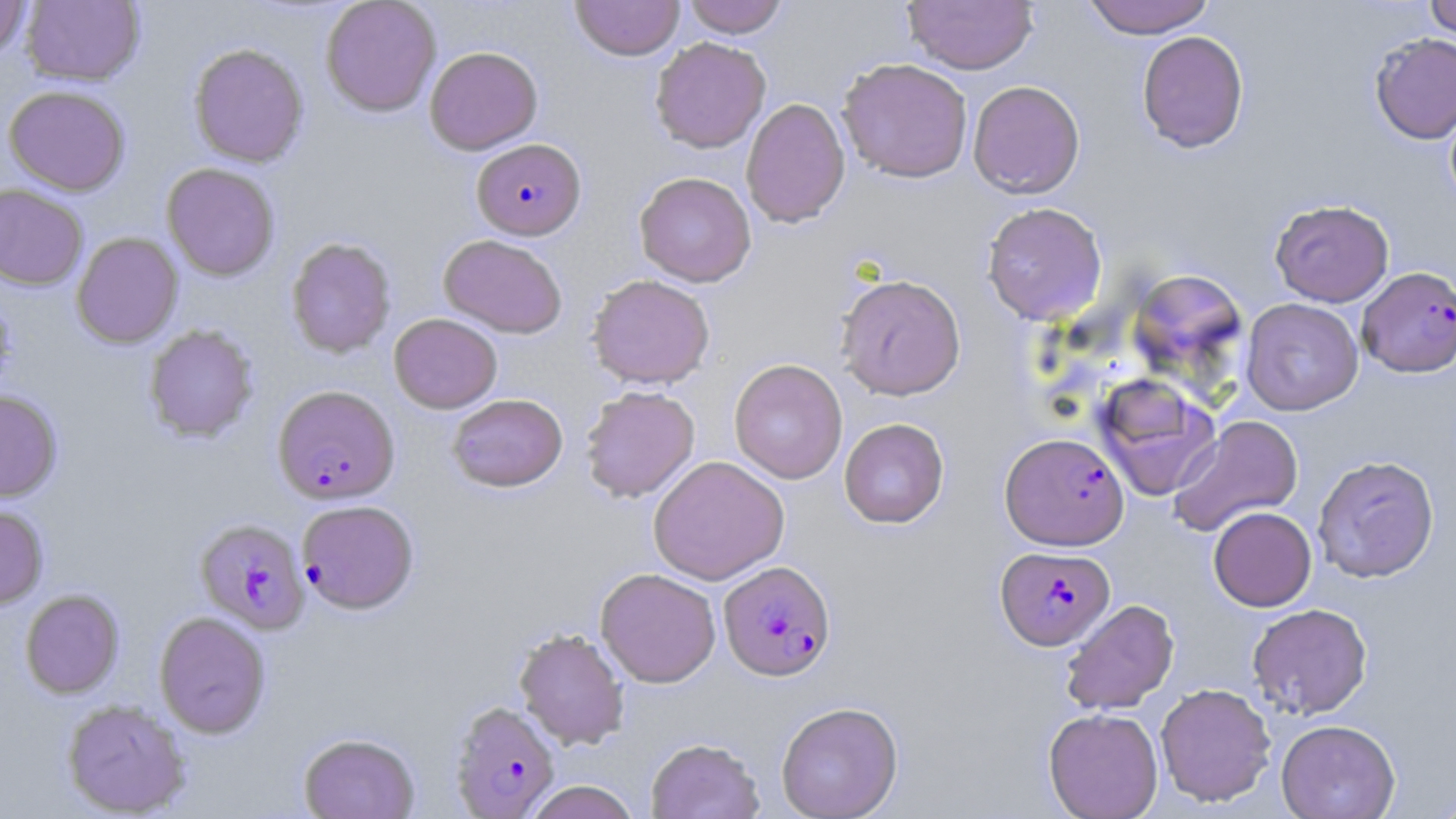

Summary:
  - Coordinate format: approximate bounding boxes as (x1, y1, x2, y2) in pixels
  - Uninfected red blood cell locations: (0, 0, 32, 61), (320, 0, 442, 117), (571, 0, 684, 61), (682, 0, 790, 37), (1082, 0, 1215, 38), (1423, 0, 1456, 41), (21, 1, 144, 87), (902, 1, 1038, 74), (1136, 31, 1249, 153), (1369, 32, 1456, 144), (650, 36, 771, 153), (189, 43, 309, 167), (425, 46, 542, 154), (837, 58, 974, 183), (968, 80, 1085, 199), (4, 85, 131, 195), (740, 97, 850, 228), (162, 163, 281, 281), (634, 172, 756, 287), (0, 183, 88, 290), (1270, 199, 1394, 307), (981, 202, 1108, 325), (71, 232, 183, 348), (438, 234, 568, 338), (286, 237, 396, 358), (1127, 268, 1249, 389), (835, 273, 966, 400), (587, 274, 715, 390), (1241, 298, 1364, 415), (389, 313, 502, 413), (144, 324, 259, 442), (729, 358, 848, 484), (1093, 375, 1221, 500), (580, 386, 700, 503), (0, 390, 62, 502), (447, 393, 568, 492), (1169, 415, 1304, 537), (839, 418, 949, 528), (1313, 455, 1440, 582), (648, 456, 789, 584), (0, 504, 49, 609), (1208, 506, 1316, 611), (596, 568, 721, 687), (20, 589, 124, 698), (1060, 599, 1179, 715), (1247, 603, 1373, 719), (154, 611, 271, 738), (514, 627, 630, 750), (1155, 683, 1276, 807), (61, 699, 191, 817), (776, 701, 903, 819), (1043, 707, 1163, 819), (1276, 719, 1401, 818), (298, 732, 420, 818), (646, 737, 764, 818), (523, 781, 641, 819), (1430, 783, 1456, 819)
  - Plasmodium falciparum-infected red blood cell locations: (472, 138, 587, 240), (1357, 267, 1456, 377), (273, 385, 400, 504), (1000, 432, 1129, 550), (297, 500, 419, 614), (195, 518, 310, 634), (996, 546, 1115, 650), (719, 560, 835, 681), (449, 701, 561, 818)
  - Slide-level diagnosis: Plasmodium falciparum
  - Field of view: single
  - Stain: May-Grünwald-Giemsa
  - Modality: optical microscopy
  - Image size: 1456×819 pixels
  - Magnification: 1000x
  - Preparation: thin blood film